Give the extent of all Plasmodium malariae-infected red blood cells.
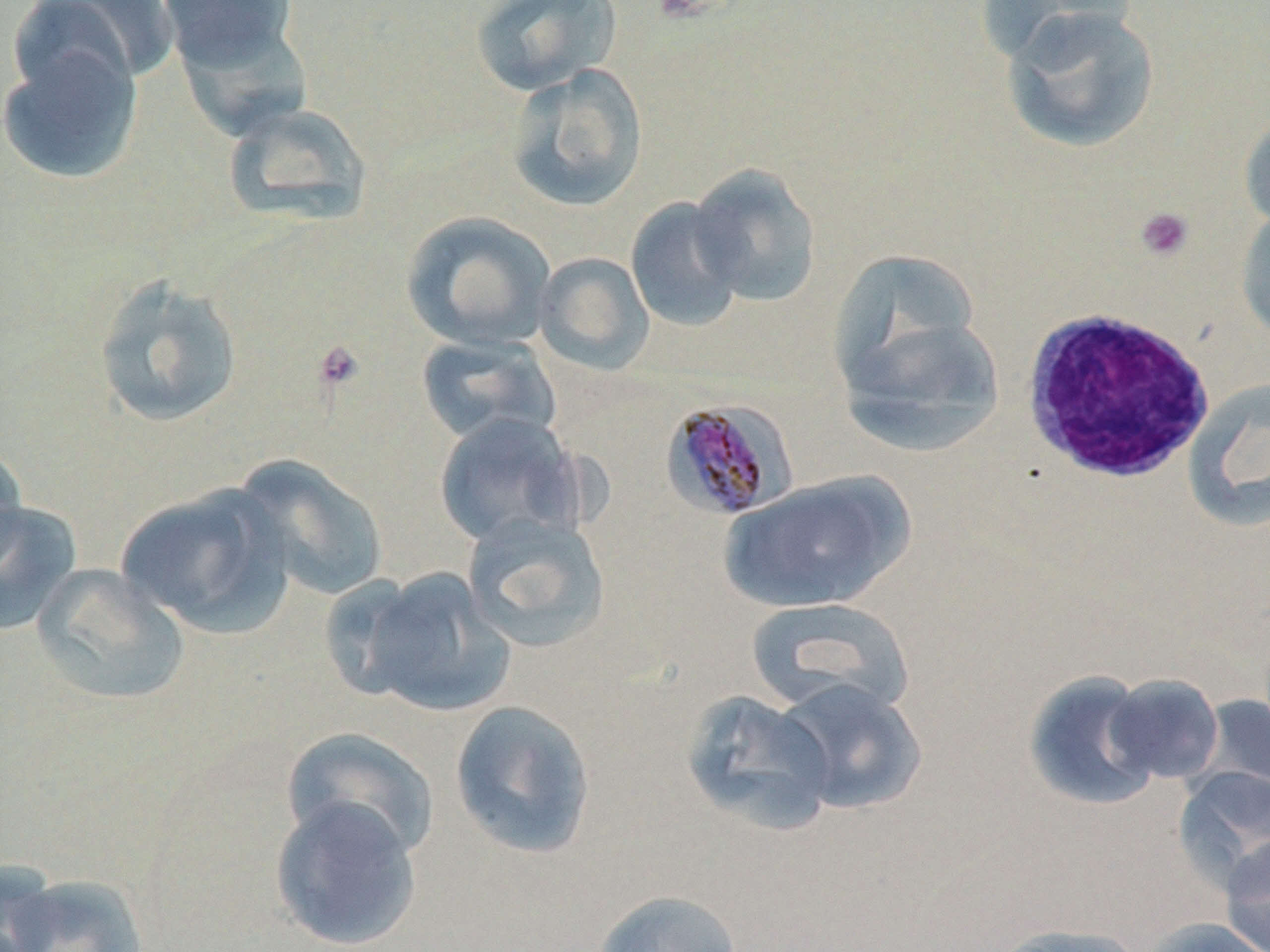
Approximate bounding boxes as [x1, y1, x2, y2] in pixels.
Plasmodium malariae-infected red blood cells: [660, 398, 798, 522].

Summary:
  - Uninfected red blood cell locations: [5, 0, 174, 99], [156, 0, 301, 75], [469, 0, 622, 97], [978, 0, 1142, 67], [1000, 5, 1162, 153], [166, 10, 312, 136], [0, 40, 145, 186], [504, 61, 649, 212], [221, 101, 373, 228], [1238, 107, 1270, 235], [688, 163, 823, 308], [624, 196, 747, 332], [1235, 206, 1270, 344], [400, 210, 557, 352], [827, 247, 986, 399], [533, 251, 655, 375], [92, 274, 244, 430], [838, 308, 1006, 458], [415, 333, 561, 446], [1184, 376, 1270, 531], [433, 411, 587, 549], [0, 435, 28, 580], [232, 454, 391, 602], [721, 472, 912, 614], [114, 483, 293, 638], [0, 499, 83, 637], [461, 513, 612, 653], [32, 564, 190, 706], [350, 567, 516, 717], [744, 596, 916, 718], [1023, 668, 1163, 813], [1103, 673, 1225, 784], [772, 676, 928, 815], [680, 689, 837, 837], [1196, 693, 1270, 804], [449, 699, 597, 860], [281, 726, 440, 861], [1174, 766, 1270, 885], [268, 795, 422, 951], [1219, 833, 1270, 952], [0, 863, 61, 952], [3, 873, 150, 952], [592, 889, 743, 951], [1138, 917, 1270, 952], [989, 923, 1147, 952]
  - Platelet locations: [1135, 206, 1195, 262], [312, 340, 366, 394]
  - White blood cell locations: [1020, 304, 1219, 486]
  - Slide-level diagnosis: Plasmodium malariae
  - Image size: 1270×952 pixels
  - Preparation: thin blood smear
  - Modality: optical microscopy
  - Magnification: 1000x
  - Stain: May-Grünwald-Giemsa
  - Field of view: one of a larger specimen